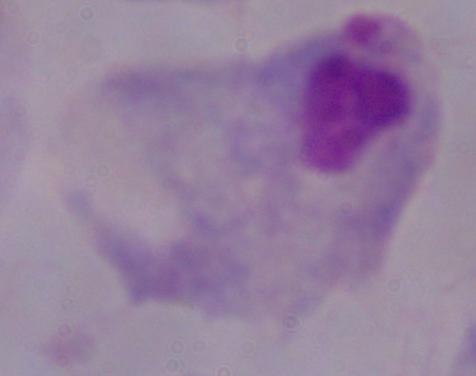
modality: micrograph
magnification: 1000x
identification: trichomonad